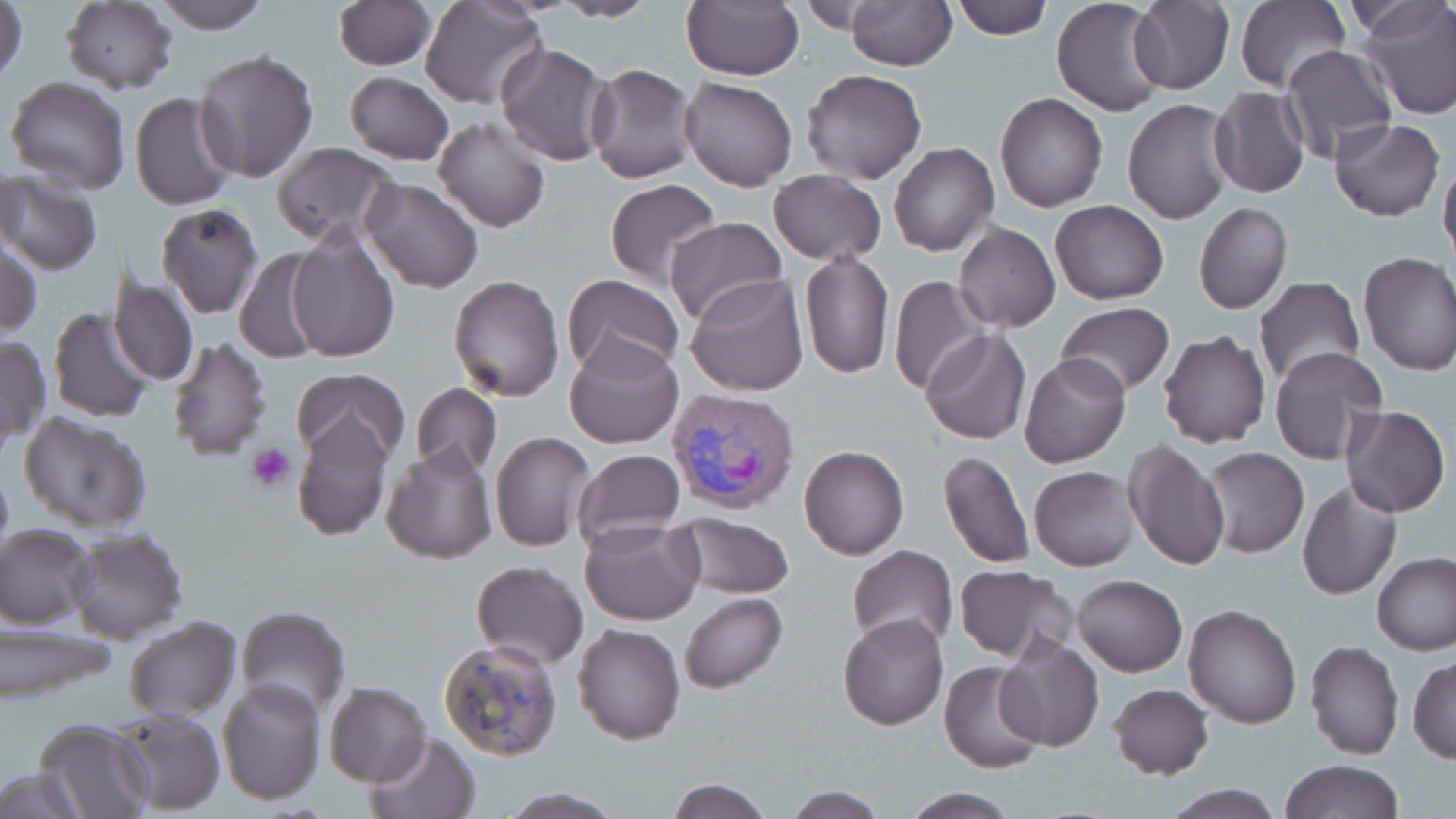

slide_level_diagnosis: Plasmodium vivax
magnification: 1000x
preparation: thin blood smear
platelet_locations: 'approximate bounding boxes as (x1,y1)-(x2,y2) corner pairs in pixels: (245,443)-(296,493)'
stain: May-Grünwald-Giemsa
image_size: 1456×819 pixels
field_of_view: one of a larger specimen
uninfected_red_blood_cell_locations: 'approximate bounding boxes as (x1,y1)-(x2,y2) corner pairs in pixels: (0,0)-(28,88), (152,0)-(273,31), (421,0)-(545,109), (679,0)-(803,82), (950,0)-(1052,40), (1050,0)-(1170,118), (60,1)-(178,94), (333,1)-(435,70), (549,1)-(660,22), (845,1)-(957,70), (1129,1)-(1234,93), (1236,1)-(1350,93), (1360,3)-(1456,119), (494,42)-(614,166), (1280,45)-(1397,163), (192,49)-(319,184), (585,63)-(697,183), (799,69)-(928,185), (345,71)-(453,165), (6,76)-(131,193), (680,76)-(797,190), (1209,86)-(1309,199), (130,91)-(241,211), (995,92)-(1107,212), (1124,98)-(1234,225), (433,116)-(551,234), (1331,117)-(1444,221), (889,141)-(998,257), (270,142)-(400,248), (1439,154)-(1456,265), (1,168)-(28,263), (768,170)-(886,265), (2,174)-(102,275), (360,177)-(485,293), (604,178)-(721,288), (1050,201)-(1169,306), (1194,203)-(1292,316), (157,205)-(262,319), (663,215)-(789,328), (954,221)-(1060,332), (284,230)-(400,364), (2,240)-(41,339), (233,247)-(328,364), (798,251)-(894,378), (1358,252)-(1456,376), (107,273)-(200,387), (563,274)-(686,381), (685,274)-(809,396), (446,275)-(565,402), (888,276)-(988,395), (1253,278)-(1364,389), (1057,302)-(1174,399), (47,306)-(157,424), (1158,329)-(1271,447), (922,330)-(1031,444), (167,335)-(274,461), (565,335)-(684,449), (0,336)-(51,446), (1269,347)-(1388,465), (1019,352)-(1130,468), (291,369)-(409,469), (411,382)-(501,479), (1343,405)-(1450,517), (18,412)-(152,534), (292,417)-(394,542), (490,430)-(598,552), (1123,440)-(1229,572), (382,445)-(497,564), (799,445)-(910,561), (1200,446)-(1309,559), (938,447)-(1034,569), (572,450)-(687,548), (0,461)-(14,567), (1029,465)-(1141,571), (1296,481)-(1401,599), (671,513)-(796,598), (579,518)-(704,625), (2,523)-(97,628), (65,529)-(188,643), (847,546)-(959,652), (1373,552)-(1456,656), (471,559)-(588,669), (953,565)-(1078,665), (1072,574)-(1187,676), (680,592)-(787,693), (1184,604)-(1302,729), (234,605)-(351,718), (837,612)-(950,730), (123,616)-(240,723), (572,622)-(686,745), (3,626)-(116,706), (437,635)-(565,762), (1304,639)-(1404,759), (997,641)-(1102,751), (1408,655)-(1456,763), (939,659)-(1049,772), (217,680)-(326,805), (322,681)-(431,787), (1107,684)-(1213,780), (111,708)-(226,814), (34,718)-(155,819), (366,731)-(480,818), (1280,758)-(1404,819), (0,770)-(87,816), (663,777)-(775,818), (1162,784)-(1285,818), (781,786)-(889,817), (496,787)-(623,817), (898,787)-(1023,816)'
modality: light microscopy
plasmodium_vivax_infected_red_blood_cell_locations: 'approximate bounding boxes as (x1,y1)-(x2,y2) corner pairs in pixels: (667,386)-(803,517)'